Assess for Plasmodium parasites.
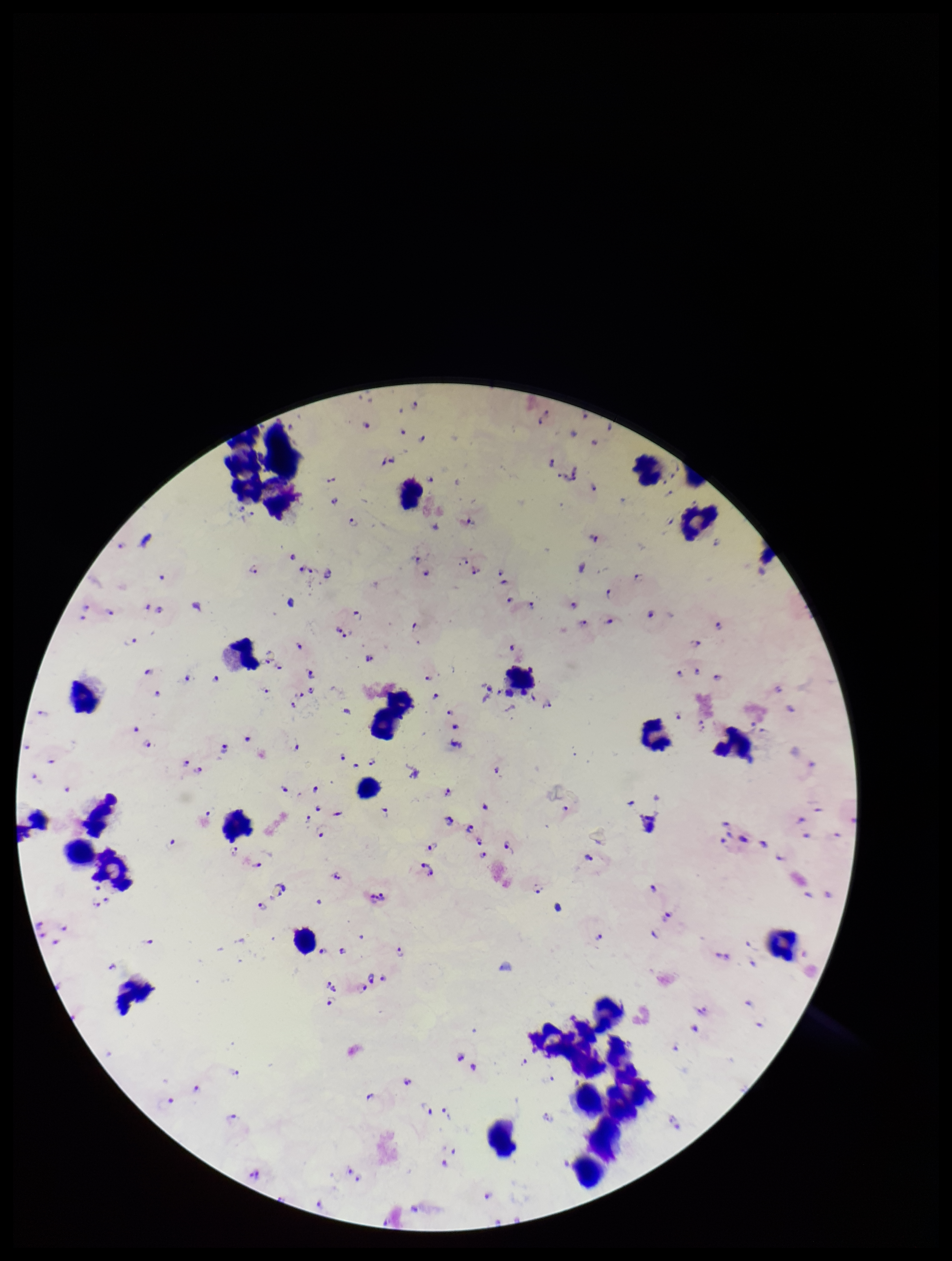
Seen.

Image is 952×1261 pixels. Leukocyte count: 29. One field from this slide. Stained with Giemsa. Species reported for this patient: Plasmodium falciparum. Patient malaria status: infected. Preparation: thick smear. Parasite count: 108. Photographed through the microscope eyepiece with a smartphone camera.